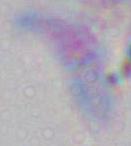 Toxoplasma gondii is seen. Photomicrograph. 1000x magnification.